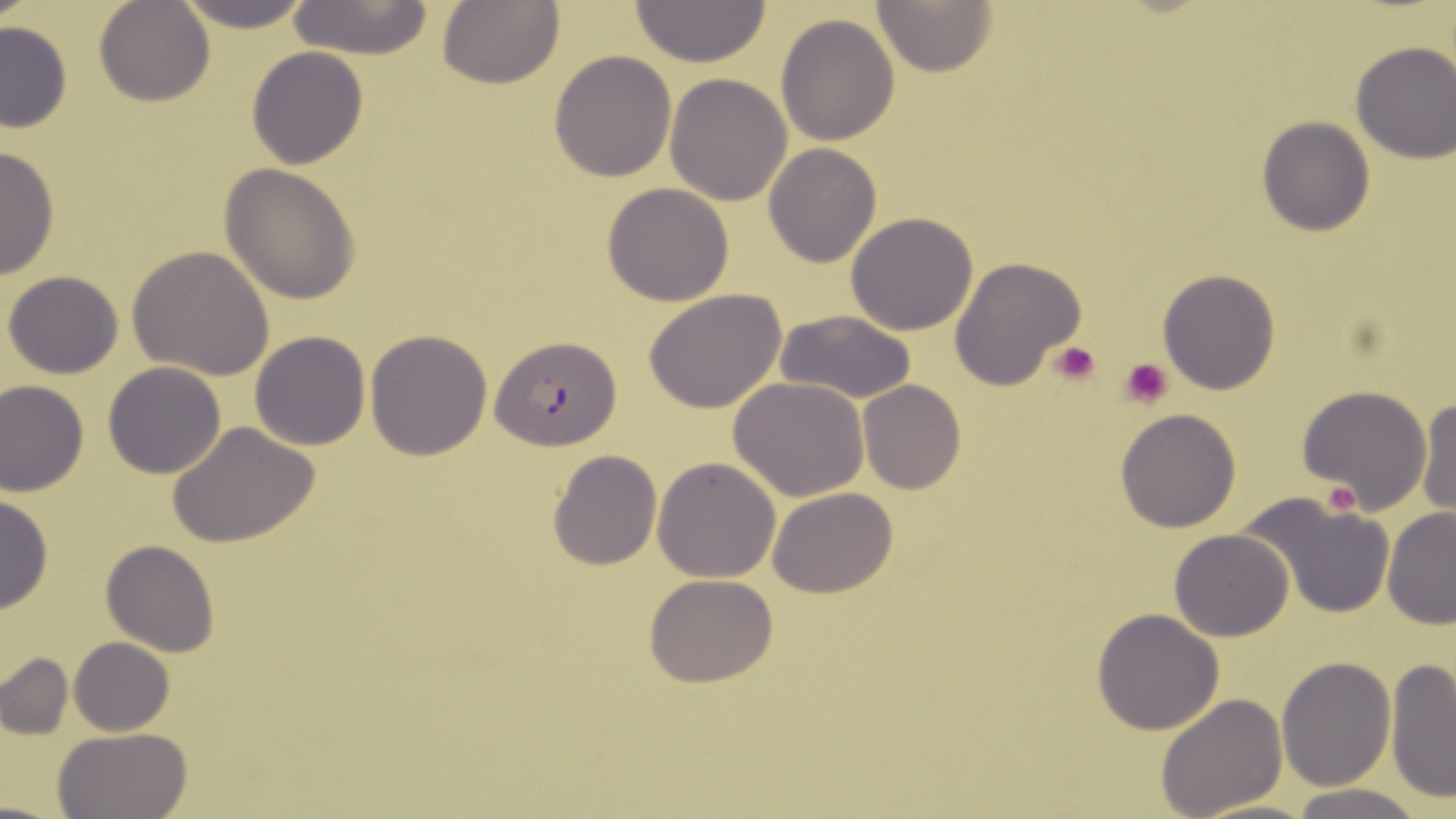

Summary:
  - Coordinate format: approximate bounding boxes as [x1, y1, x2, y2] in pixels
  - Uninfected red blood cell locations: [0, 0, 38, 28], [94, 0, 216, 107], [175, 0, 316, 30], [437, 0, 564, 89], [285, 1, 434, 59], [872, 1, 997, 76], [629, 2, 772, 68], [776, 14, 900, 147], [0, 20, 72, 133], [1349, 41, 1456, 164], [246, 46, 369, 170], [549, 49, 677, 182], [664, 73, 793, 207], [1257, 117, 1374, 236], [763, 142, 882, 268], [0, 144, 59, 283], [220, 164, 362, 304], [602, 182, 734, 306], [169, 189, 340, 337], [845, 212, 980, 336], [127, 246, 276, 381], [950, 256, 1086, 394], [1157, 269, 1283, 395], [5, 270, 124, 378], [643, 288, 786, 414], [774, 310, 919, 404], [250, 330, 371, 451], [366, 330, 493, 461], [103, 362, 228, 479], [729, 377, 872, 501], [1, 380, 88, 496], [859, 381, 967, 495], [1298, 384, 1433, 512], [1358, 391, 1456, 519], [1413, 395, 1455, 518], [1115, 408, 1240, 532], [169, 421, 320, 550], [547, 449, 662, 570], [652, 456, 781, 581], [768, 487, 899, 599], [0, 492, 53, 615], [1240, 494, 1397, 619], [1382, 506, 1456, 630], [1168, 530, 1293, 642], [101, 540, 219, 657], [645, 573, 778, 688], [1091, 608, 1226, 735], [69, 638, 175, 735], [1, 654, 72, 739], [1277, 657, 1395, 791], [1385, 657, 1456, 802], [1156, 693, 1289, 818], [52, 728, 191, 818], [1288, 783, 1426, 819], [1190, 799, 1324, 819]
  - Platelet locations: [1048, 342, 1102, 384], [1119, 357, 1174, 409], [1316, 482, 1361, 517]
  - Plasmodium falciparum-infected red blood cell locations: [491, 336, 623, 449]
  - Slide-level diagnosis: Plasmodium falciparum
  - Image size: 1456×819 pixels
  - Stain: May-Grünwald-Giemsa
  - Preparation: thin blood film
  - Field of view: one of a larger specimen
  - Magnification: 1000x
  - Modality: optical microscopy